Classify this cell by malaria status.
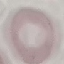
It is uninfected.

Summary:
  - Capture: smartphone through the microscope eyepiece
  - Stain: Giemsa
  - Image type: cell patch, automatically extracted from a larger field of view and resized to 64 × 64 pixels
  - Preparation: thin smear